Name the blood parasite species.
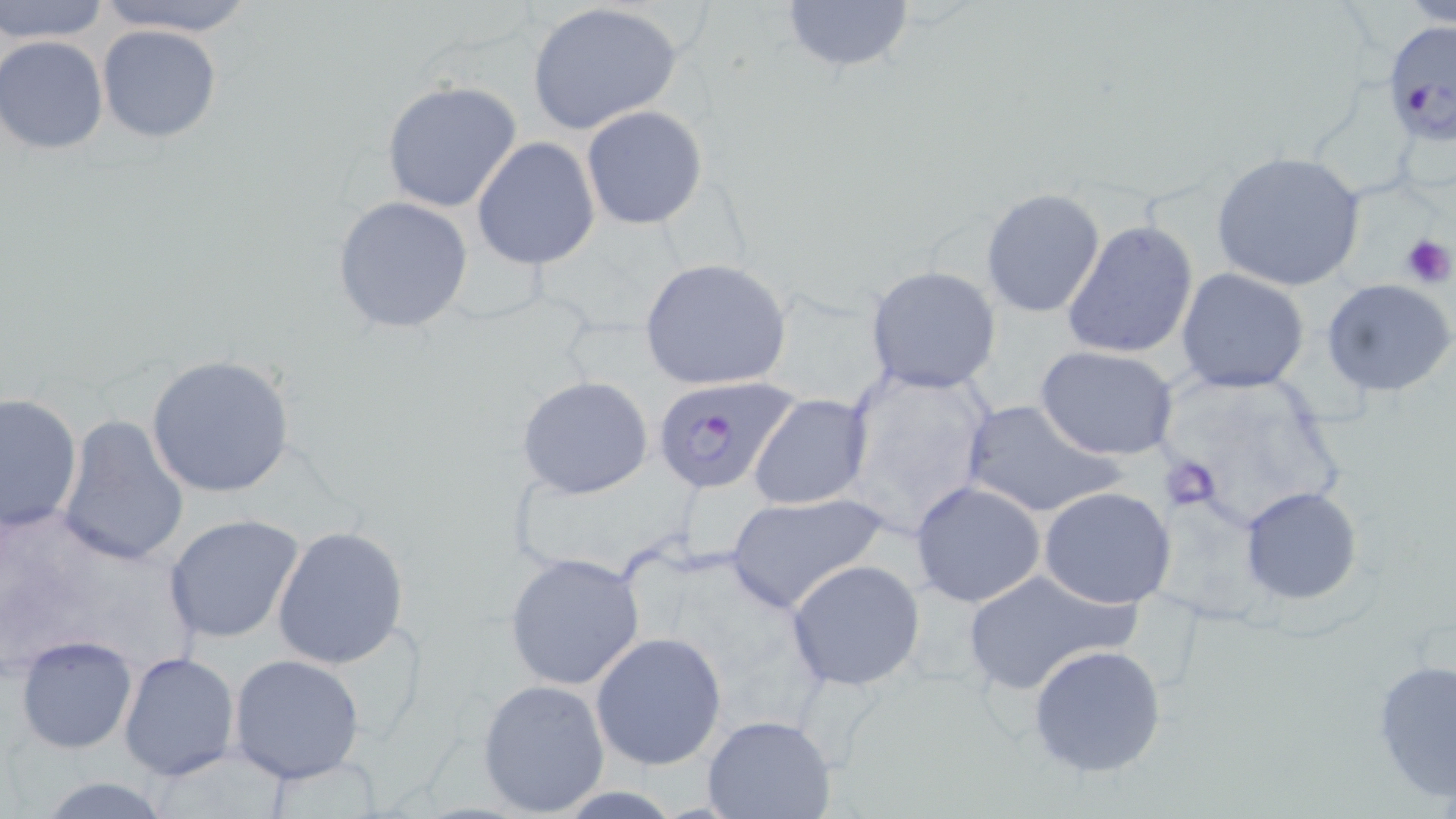
Plasmodium falciparum.

{
  "platelet_locations": "approximate bounding boxes as (x1,y1)-(x2,y2) corner pairs in pixels: (1400,232)-(1453,290), (1157,456)-(1217,512)",
  "plasmodium_falciparum_infected_red_blood_cell_locations": "approximate bounding boxes as (x1,y1)-(x2,y2) corner pairs in pixels: (1383,23)-(1455,145), (651,374)-(800,497)",
  "stain": "May-Grünwald-Giemsa",
  "field_of_view": "single",
  "preparation": "thin blood film",
  "uninfected_red_blood_cell_locations": "approximate bounding boxes as (x1,y1)-(x2,y2) corner pairs in pixels: (2,0)-(110,44), (91,0)-(264,36), (778,0)-(915,77), (1402,0)-(1456,27), (528,2)-(685,136), (96,24)-(222,143), (0,36)-(111,155), (381,80)-(524,215), (581,106)-(707,230), (472,138)-(600,270), (1211,150)-(1369,293), (980,189)-(1106,318), (331,195)-(474,334), (1061,219)-(1199,361), (640,257)-(794,392), (865,265)-(1002,394), (1176,267)-(1311,394), (1322,276)-(1455,398), (1036,346)-(1180,460), (145,354)-(297,497), (838,367)-(997,530), (517,375)-(654,499), (0,391)-(83,538), (748,393)-(873,511), (960,399)-(1126,521), (57,416)-(190,567), (910,480)-(1048,608), (1239,485)-(1361,605), (1039,487)-(1178,609), (725,491)-(889,614), (163,514)-(306,647), (271,525)-(410,669), (502,551)-(647,690), (786,559)-(926,690), (958,570)-(1138,697), (591,631)-(727,769), (13,633)-(139,755), (1026,642)-(1170,779), (118,650)-(240,782), (227,654)-(365,784), (1371,657)-(1455,803), (476,677)-(610,816), (701,715)-(838,819), (27,776)-(181,818)",
  "magnification": "1000x",
  "image_size": "1456×819 pixels",
  "modality": "optical microscopy"
}